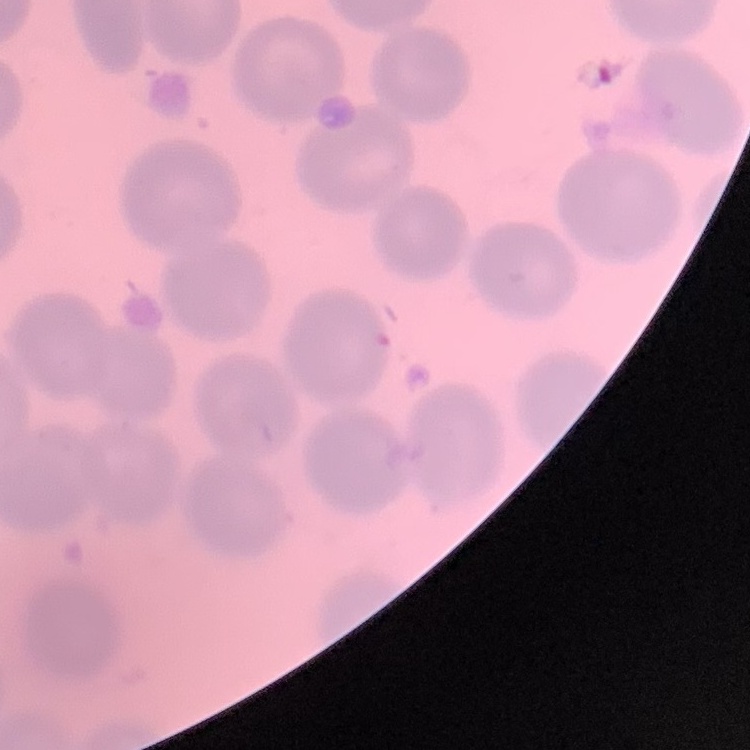
{
  "red_blood_cell_morphology": "no rouleaux formation",
  "stain": "Field's or Giemsa",
  "image_type": "one tile cut from a larger photomicrograph",
  "preparation": "thin blood film"
}